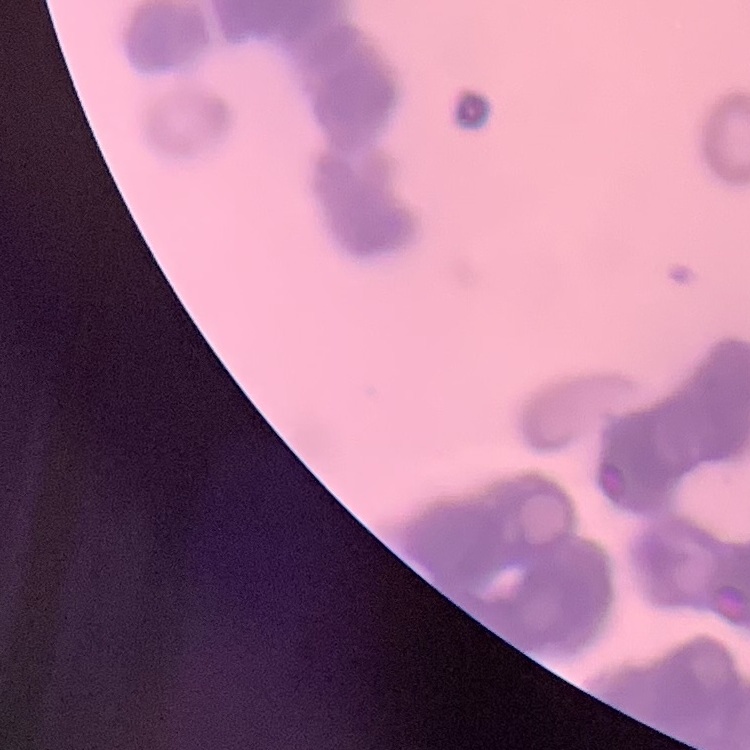

erythrocyte morphology = rouleaux formation
image type = one tile cut from a larger photomicrograph
stain = Field's or Giemsa
preparation = thin peripheral smear